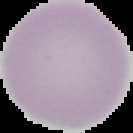
{
  "image_type": "segmented cell region on a black background",
  "result": "no malaria parasites detected",
  "preparation": "thin blood film",
  "image_size": "133×133 pixels"
}